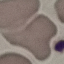

{
  "result": "no malaria parasites seen",
  "preparation": "thin blood film",
  "image_type": "cell patch, automatically extracted from a larger field of view and resized to 64 × 64 pixels",
  "stain": "Giemsa",
  "capture": "smartphone through the microscope eyepiece"
}